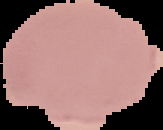

Image is 163×130 pixels. From a thin blood film. The area outside the segmented cell region is set to black. Malaria status: uninfected.